Name the parasite shown.
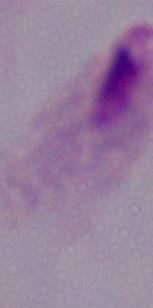
A trichomonad.

Summary:
  - Modality: photomicrograph
  - Magnification: 1000x